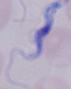

Captured at 1000x magnification. Micrograph. A trypanosome is seen.